Name the blood parasite species.
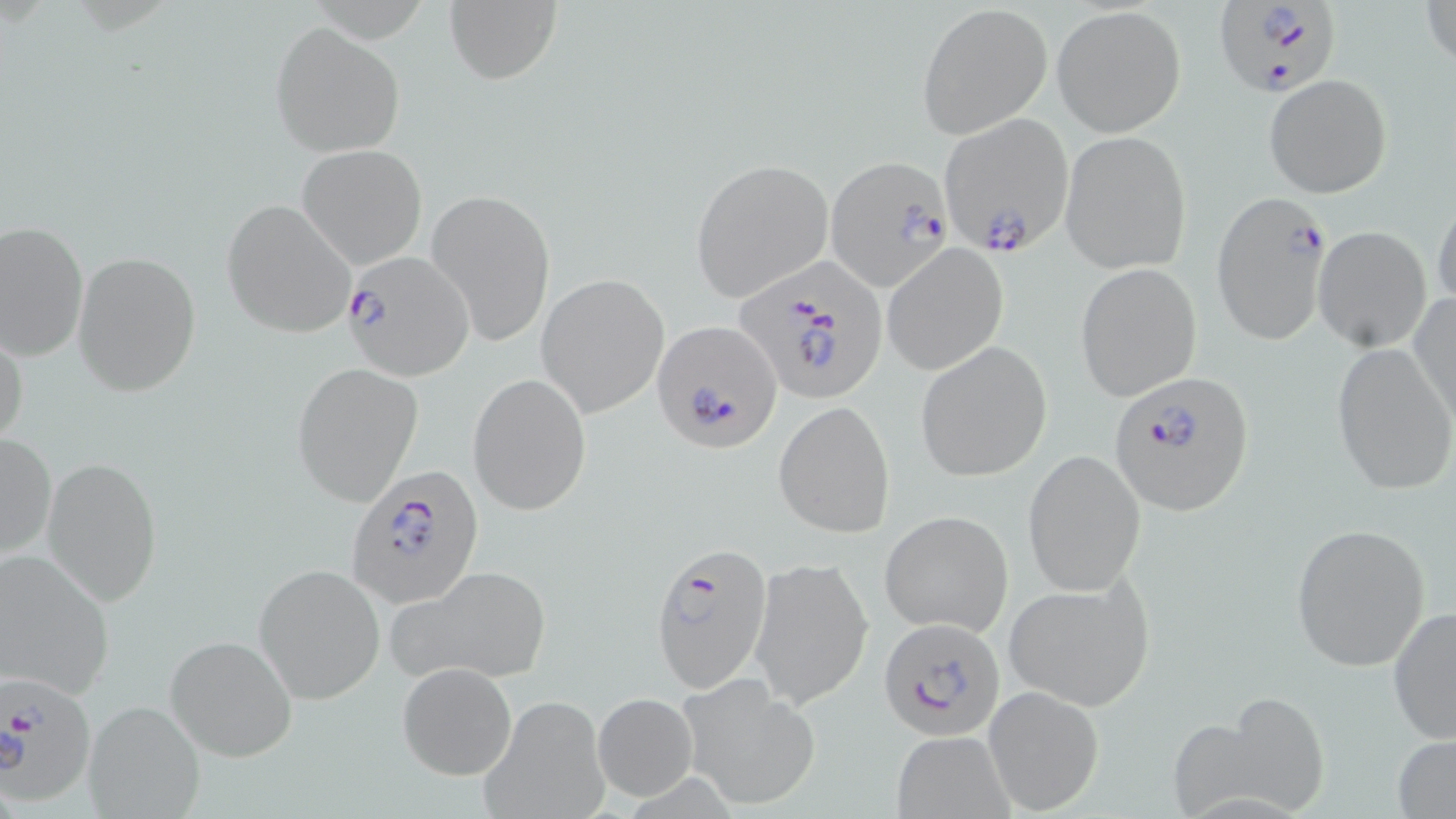
Plasmodium falciparum.

{
  "image_size": "1456×819 pixels",
  "plasmodium_falciparum_infected_red_blood_cell_locations": "approximate bounding boxes as [x1, y1, x2, y2] in pixels: [1214, 0, 1344, 100], [937, 113, 1074, 255], [827, 160, 956, 292], [1212, 190, 1333, 347], [343, 249, 473, 379], [733, 258, 889, 407], [654, 324, 782, 451], [1109, 373, 1252, 517], [348, 466, 481, 606], [651, 542, 772, 692], [880, 620, 1006, 740], [0, 670, 99, 805]",
  "uninfected_red_blood_cell_locations": "approximate bounding boxes as [x1, y1, x2, y2] in pixels: [1422, 0, 1454, 72], [443, 1, 561, 86], [919, 4, 1051, 137], [1052, 5, 1186, 136], [269, 22, 404, 158], [1265, 74, 1391, 198], [1060, 131, 1191, 274], [296, 145, 428, 269], [692, 159, 832, 300], [428, 188, 555, 347], [1431, 194, 1456, 311], [221, 199, 358, 339], [1, 221, 89, 363], [1314, 226, 1432, 352], [882, 244, 1008, 376], [71, 250, 202, 397], [1075, 261, 1202, 403], [536, 273, 669, 417], [1409, 291, 1455, 429], [0, 323, 28, 452], [1331, 343, 1455, 495], [917, 344, 1052, 481], [290, 362, 423, 507], [468, 372, 592, 517], [774, 399, 894, 538], [1, 431, 55, 564], [1024, 450, 1146, 597], [43, 456, 163, 605], [881, 510, 1014, 638], [1289, 523, 1432, 672], [0, 547, 116, 703], [748, 557, 874, 711], [385, 563, 550, 683], [253, 565, 384, 704], [1004, 578, 1155, 709], [1388, 603, 1456, 745], [164, 633, 297, 763], [398, 662, 517, 781], [677, 675, 821, 811], [982, 686, 1104, 816], [1202, 688, 1337, 818], [476, 692, 611, 819], [591, 692, 698, 801], [83, 699, 206, 819], [888, 731, 1018, 818], [1392, 736, 1456, 817]",
  "magnification": "1000x",
  "stain": "May-Grünwald-Giemsa",
  "modality": "optical microscopy",
  "preparation": "thin blood smear",
  "field_of_view": "one of a larger specimen"
}